State which parasite is depicted.
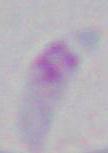
Toxoplasma gondii.

magnification: 1000x
modality: photomicrograph